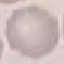

Malaria status: uninfected. Giemsa stain. Thin blood film. Photographed with a smartphone camera at the microscope eyepiece. Cell patch, automatically extracted from a larger field of view and resized to 64 × 64 pixels.